Mark where platelets are.
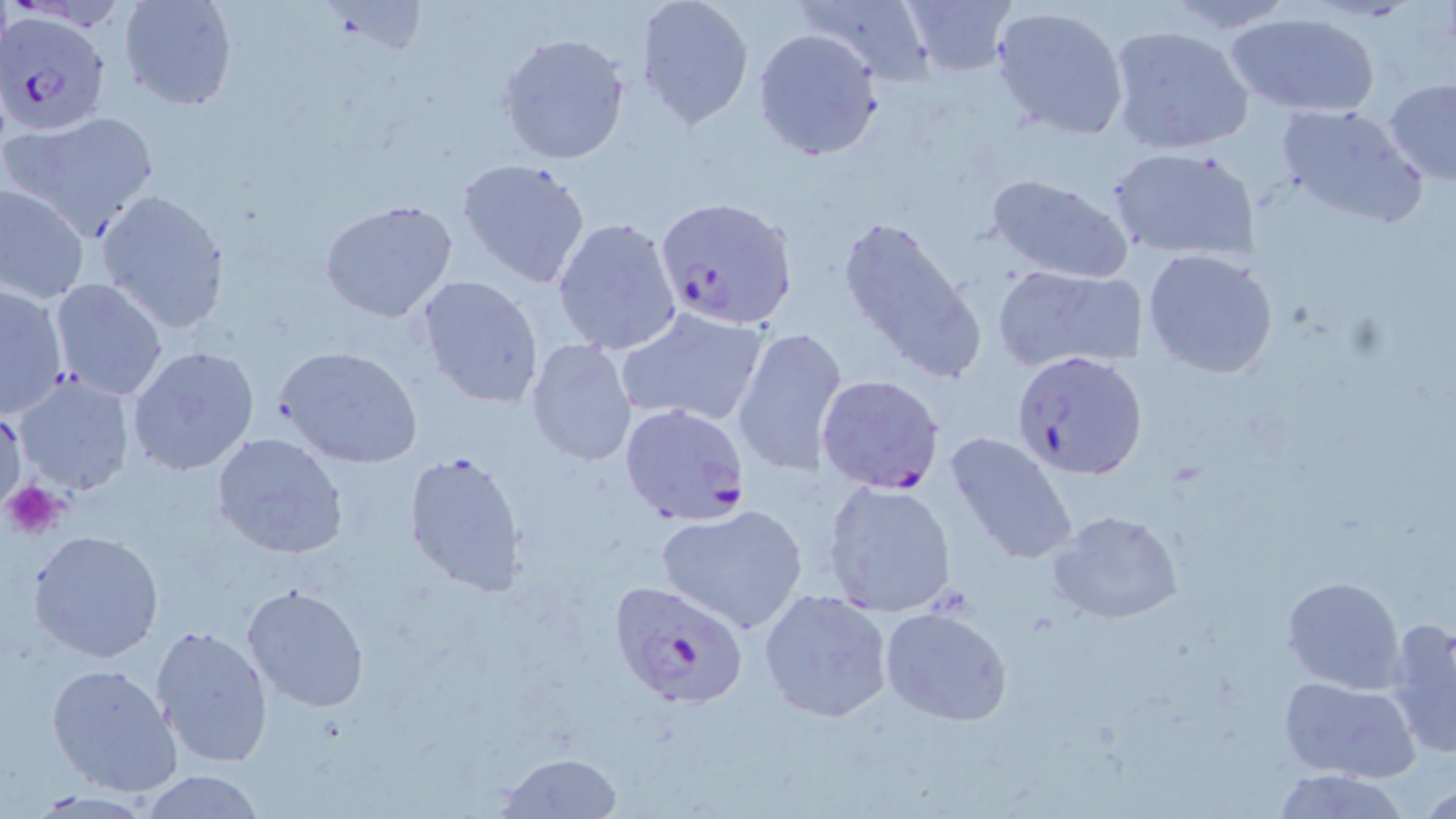
Approximate bounding boxes as named x1/y1/x2/y2 corners in pixels.
Platelets: (x1=3, y1=481, x2=63, y2=539).

slide_level_diagnosis: Plasmodium falciparum
magnification: 1000x
uninfected_red_blood_cell_locations: 'approximate bounding boxes as named x1/y1/x2/y2 corners in pixels: (x1=117, y1=0, x2=237, y2=112), (x1=635, y1=0, x2=756, y2=131), (x1=799, y1=0, x2=938, y2=83), (x1=899, y1=0, x2=1018, y2=77), (x1=1160, y1=1, x2=1298, y2=34), (x1=992, y1=5, x2=1129, y2=139), (x1=1226, y1=10, x2=1380, y2=120), (x1=1106, y1=24, x2=1254, y2=156), (x1=753, y1=27, x2=885, y2=161), (x1=498, y1=32, x2=630, y2=164), (x1=1383, y1=77, x2=1456, y2=183), (x1=1276, y1=101, x2=1425, y2=226), (x1=3, y1=111, x2=159, y2=239), (x1=1108, y1=146, x2=1258, y2=262), (x1=456, y1=156, x2=593, y2=289), (x1=985, y1=172, x2=1135, y2=283), (x1=0, y1=183, x2=90, y2=304), (x1=95, y1=189, x2=231, y2=335), (x1=319, y1=200, x2=459, y2=323), (x1=837, y1=213, x2=986, y2=383), (x1=552, y1=216, x2=683, y2=356), (x1=1141, y1=248, x2=1278, y2=379), (x1=994, y1=267, x2=1147, y2=371), (x1=414, y1=274, x2=545, y2=410), (x1=48, y1=278, x2=169, y2=402), (x1=0, y1=284, x2=71, y2=419), (x1=615, y1=305, x2=770, y2=428), (x1=733, y1=325, x2=849, y2=477), (x1=525, y1=338, x2=639, y2=469), (x1=273, y1=345, x2=423, y2=469), (x1=126, y1=346, x2=260, y2=478), (x1=11, y1=374, x2=135, y2=496), (x1=1, y1=405, x2=25, y2=512), (x1=944, y1=430, x2=1080, y2=565), (x1=211, y1=432, x2=348, y2=560), (x1=403, y1=450, x2=530, y2=596), (x1=822, y1=479, x2=959, y2=618), (x1=656, y1=504, x2=808, y2=633), (x1=1048, y1=509, x2=1184, y2=626), (x1=27, y1=529, x2=165, y2=662), (x1=1281, y1=575, x2=1406, y2=693), (x1=241, y1=583, x2=370, y2=714), (x1=759, y1=588, x2=892, y2=723), (x1=878, y1=604, x2=1013, y2=726), (x1=1383, y1=616, x2=1456, y2=762), (x1=150, y1=625, x2=273, y2=768), (x1=45, y1=663, x2=184, y2=799), (x1=1278, y1=677, x2=1423, y2=784), (x1=497, y1=752, x2=622, y2=818), (x1=1268, y1=767, x2=1410, y2=818), (x1=138, y1=769, x2=267, y2=818)'
plasmodium_falciparum_infected_red_blood_cell_locations: 'approximate bounding boxes as named x1/y1/x2/y2 corners in pixels: (x1=2, y1=9, x2=112, y2=138), (x1=656, y1=196, x2=796, y2=329), (x1=1013, y1=350, x2=1149, y2=482), (x1=815, y1=375, x2=946, y2=495), (x1=618, y1=402, x2=750, y2=525), (x1=607, y1=578, x2=751, y2=709)'
image_size: 1456×819 pixels
field_of_view: single
preparation: thin blood film
modality: light microscopy
stain: May-Grünwald-Giemsa